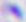

Micrograph. Toxoplasma gondii is shown. Captured at 400x magnification.